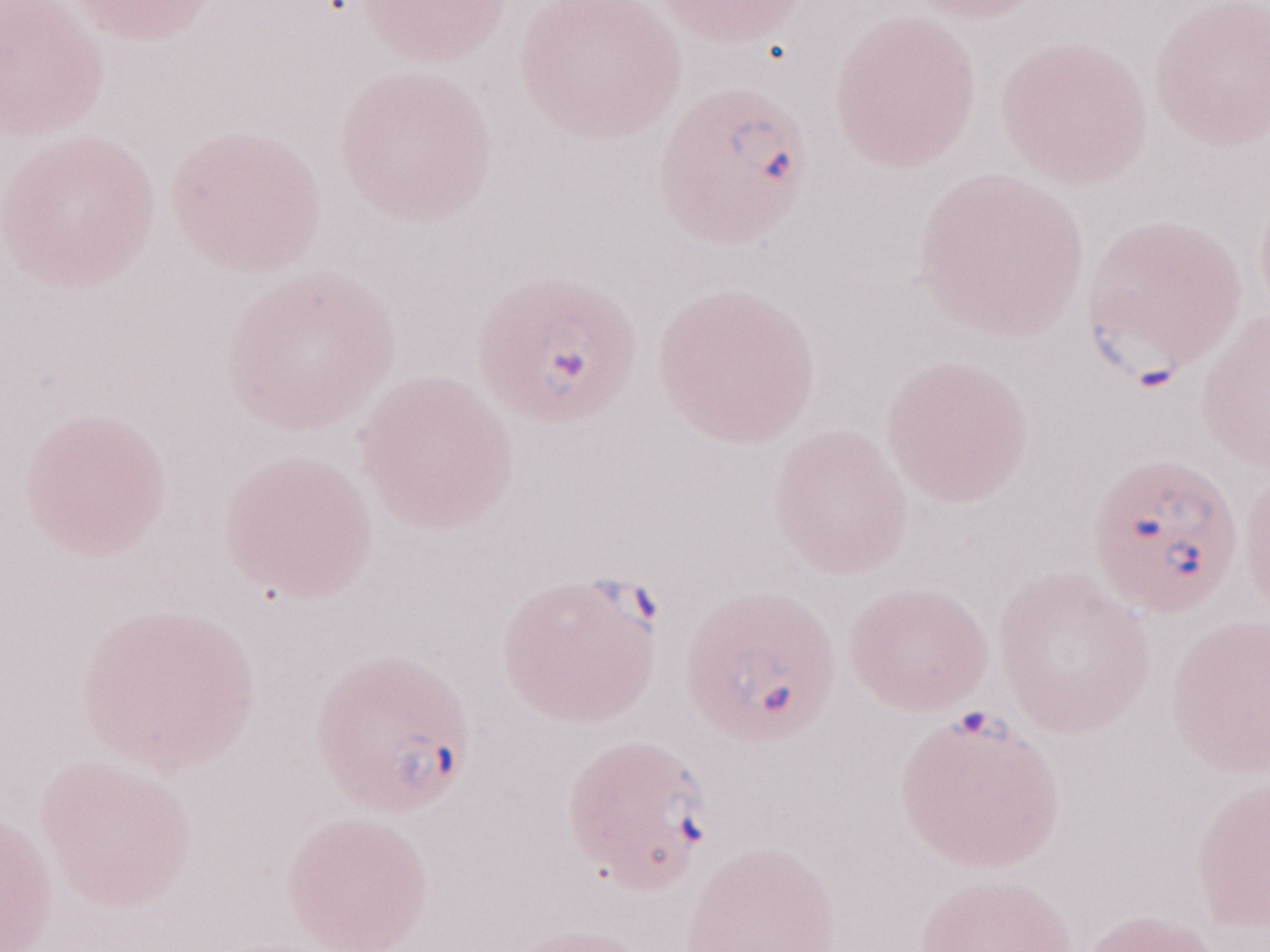 Olympus BX43 microscope and DP73 digital camera. Magnification: 1,000x. One field of this slide. Patient diagnosis: malaria infection. May-Grünwald-Giemsa (MGG) stain. Thin blood film. Image is 1270×952 pixels.